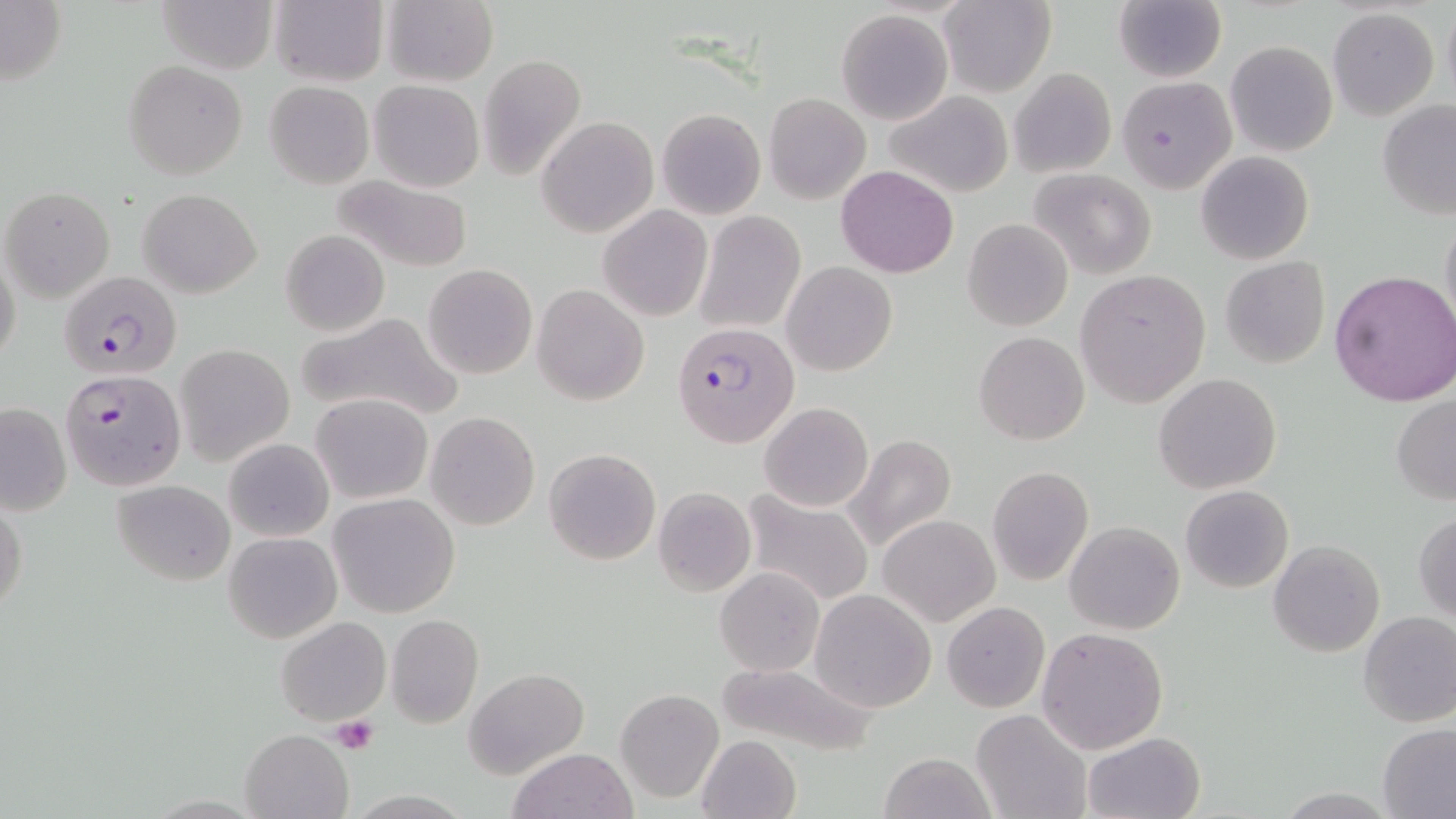
Summary:
  - Coordinate format: approximate bounding boxes as (x1,y1)-(x2,y2) corner pairs in pixels
  - Platelet locations: (330,715)-(379,756)
  - Plasmodium falciparum-infected red blood cell locations: (59,269)-(182,382), (672,321)-(799,449), (60,369)-(186,492)
  - Uninfected red blood cell locations: (154,0)-(278,73), (384,0)-(499,87), (939,0)-(1055,97), (1113,0)-(1226,83), (267,1)-(388,87), (0,2)-(67,86), (1327,8)-(1440,121), (836,9)-(953,124), (1225,40)-(1337,156), (477,53)-(587,180), (124,60)-(248,180), (1009,67)-(1117,178), (1116,75)-(1236,193), (369,79)-(485,192), (264,81)-(374,188), (883,89)-(1014,199), (763,93)-(871,205), (1376,99)-(1455,220), (656,107)-(766,220), (537,117)-(657,238), (1196,151)-(1314,265), (836,164)-(959,278), (1030,169)-(1158,278), (330,174)-(477,273), (2,185)-(115,304), (138,188)-(262,297), (598,204)-(712,321), (696,212)-(805,334), (1440,212)-(1456,335), (961,219)-(1073,332), (280,229)-(389,337), (0,249)-(22,375), (1220,257)-(1330,370), (781,261)-(898,377), (423,264)-(538,380), (1075,269)-(1210,406), (1329,270)-(1456,408), (532,284)-(648,405), (297,310)-(466,424), (973,331)-(1089,444), (175,344)-(295,467), (1154,372)-(1280,493), (312,393)-(433,504), (1390,395)-(1456,504), (1,402)-(71,516), (759,402)-(872,513), (426,411)-(540,530), (844,433)-(956,550), (224,438)-(333,541), (544,448)-(661,566), (987,466)-(1094,585), (110,479)-(236,585), (1180,485)-(1294,593), (654,486)-(755,596), (742,491)-(875,607), (1,492)-(27,619), (328,493)-(460,617), (1413,511)-(1456,622), (878,514)-(1000,625), (1065,521)-(1184,634), (225,532)-(342,644), (1267,538)-(1384,657), (715,568)-(824,675), (810,588)-(935,712), (942,601)-(1048,712), (1358,611)-(1456,728), (385,613)-(484,728), (275,616)-(391,727), (1037,626)-(1168,752), (712,662)-(877,758), (465,668)-(587,776), (614,689)-(724,803), (971,707)-(1091,819), (1377,724)-(1456,817), (240,728)-(354,819), (1083,731)-(1206,818), (695,734)-(800,819), (507,747)-(635,819), (878,752)-(993,819)
  - Slide-level diagnosis: Plasmodium falciparum
  - Stain: May-Grünwald-Giemsa
  - Preparation: thin blood smear
  - Image size: 1456×819 pixels
  - Modality: light microscopy
  - Field of view: one of a larger specimen
  - Magnification: 1000x